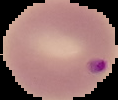

Summary:
  - Image size: 118×100 pixels
  - Preparation: thin blood film
  - Image type: segmented cell region with the area outside set to black
  - Result: Plasmodium parasites identified